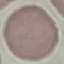

{
  "malaria_status": "uninfected",
  "stain": "Giemsa",
  "image_type": "automatically extracted cell patch, resized to 64 × 64 pixels",
  "preparation": "thin smear",
  "capture": "smartphone through the microscope eyepiece"
}